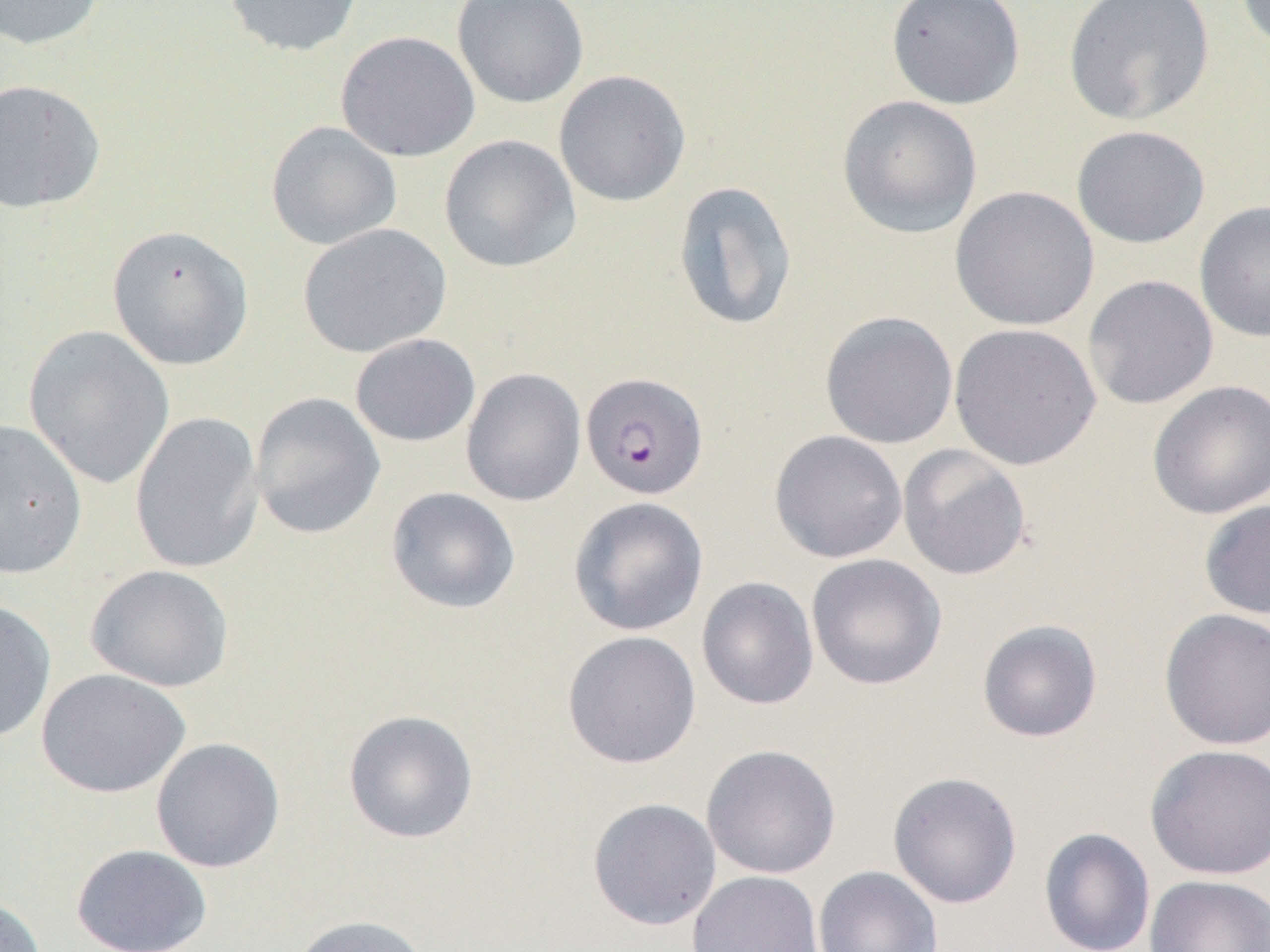
Approximate bounding boxes as (x1,y1)-(x2,y2) corner pairs in pixels. Plasmodium falciparum-infected red blood cell locations: (580,371)-(709,500). Uninfected red blood cell locations: (0,0)-(107,50), (221,0)-(363,57), (451,0)-(589,108), (886,0)-(1026,109), (1062,0)-(1215,126), (1234,0)-(1270,52), (336,30)-(480,162), (553,69)-(691,207), (0,78)-(106,214), (837,95)-(983,239), (265,121)-(402,250), (1071,125)-(1211,249), (439,135)-(582,273), (672,180)-(799,332), (950,186)-(1099,331), (1194,200)-(1270,343), (297,223)-(452,358), (107,224)-(254,370), (1082,274)-(1219,410), (819,310)-(959,449), (949,323)-(1101,470), (24,324)-(175,490), (350,333)-(481,447), (461,368)-(586,507), (1147,380)-(1270,519), (249,392)-(385,540), (129,410)-(265,575), (0,419)-(87,579), (769,429)-(908,563), (897,444)-(1033,581), (385,486)-(521,614), (568,496)-(709,636), (1198,499)-(1270,620), (805,553)-(947,691), (85,564)-(235,692), (696,576)-(819,710), (0,599)-(57,743), (1158,608)-(1270,751), (976,619)-(1103,743), (562,630)-(702,770), (36,668)-(190,798), (343,709)-(479,844), (150,737)-(286,873), (1144,743)-(1270,881), (701,744)-(841,880), (887,770)-(1023,908), (587,798)-(722,930), (1039,827)-(1156,952), (71,844)-(213,952), (812,865)-(943,952), (686,870)-(825,952), (1145,874)-(1270,952), (0,893)-(47,952), (287,914)-(432,952). Slide-level diagnosis: Plasmodium falciparum. Thin blood film. Image is 1270×952 pixels. Optical microscopy. 1000x magnification. Single field of view.